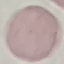
Malaria status: uninfected. Thin blood film. Automatically extracted cell patch, resized to 64 × 64 pixels. Photographed with a smartphone camera at the microscope eyepiece. Giemsa-stained preparation.